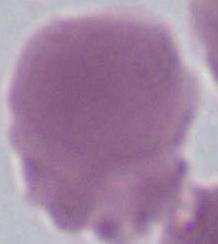
Summary:
  - Magnification: 1000x
  - Identification: erythrocyte
  - Modality: photomicrograph